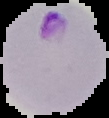
From a thin blood film. Image is 109×118 pixels. Segmented cell region on a black background. Result: Plasmodium parasites identified.